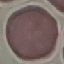

Summary:
  - Result: no malaria parasites detected
  - Preparation: thin blood smear
  - Capture: smartphone through the microscope eyepiece
  - Image type: cell patch, automatically extracted from a larger field of view and resized to 64 × 64 pixels
  - Stain: Giemsa